Locate every blood parasite and identify its species.
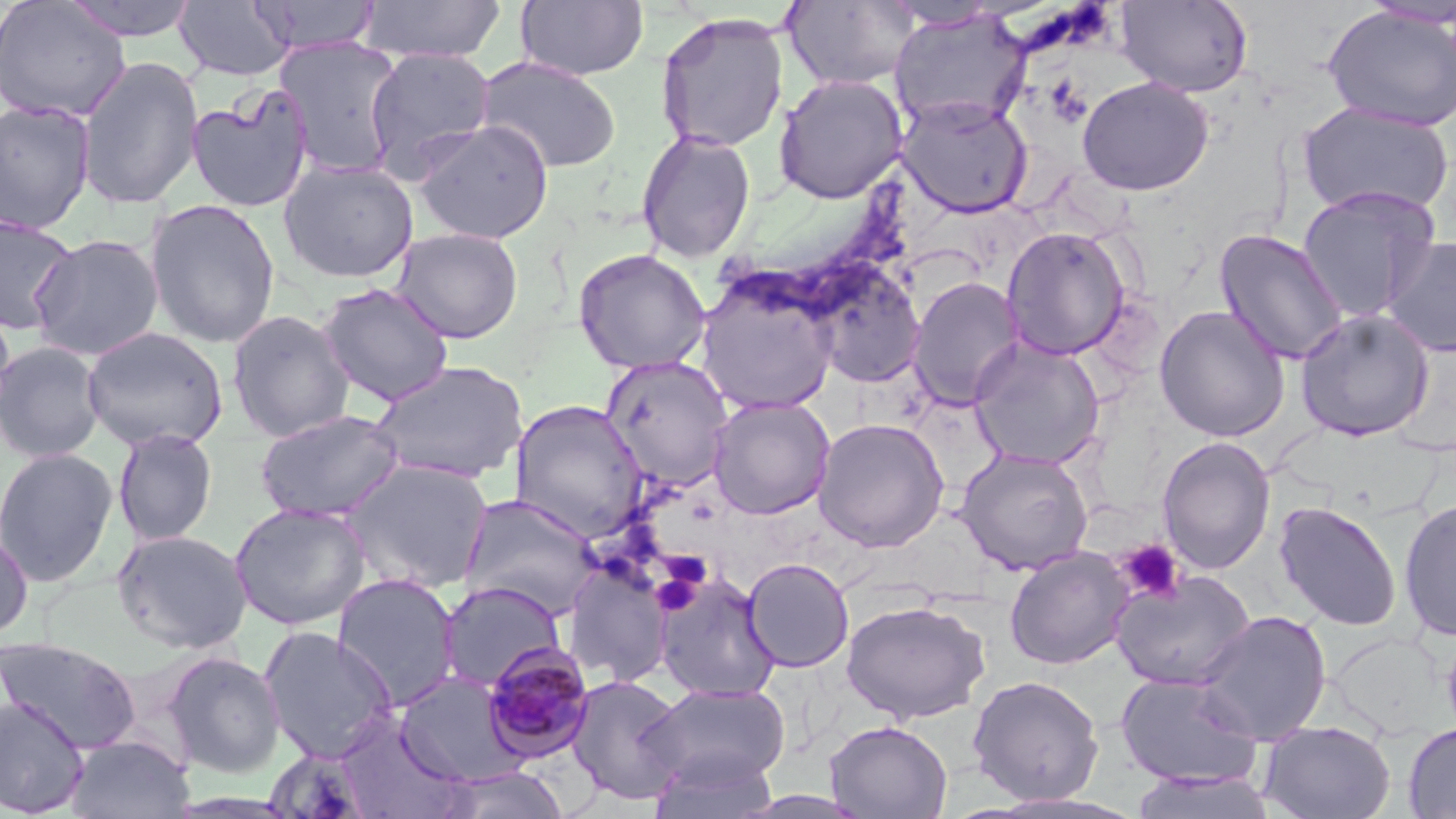
Approximate bounding boxes as [x1, y1, x2, y2] in pixels.
Plasmodium malariae-infected red blood cells: [481, 641, 595, 762].
No Plasmodium falciparum, Plasmodium ovale, Plasmodium vivax, Babesia divergens, or Trypanosoma brucei observed.

slide_level_diagnosis: Plasmodium malariae
preparation: thin blood smear
field_of_view: one of a larger specimen
uninfected_red_blood_cell_locations: 'approximate bounding boxes as [x1, y1, x2, y2] in pixels: [62, 0, 202, 42], [356, 0, 507, 62], [515, 0, 649, 81], [783, 0, 920, 91], [0, 1, 131, 124], [175, 1, 294, 82], [249, 1, 382, 55], [1115, 1, 1254, 97], [881, 2, 1009, 30], [1322, 4, 1456, 132], [889, 9, 1031, 133], [654, 11, 790, 154], [274, 36, 406, 177], [363, 46, 498, 181], [77, 56, 204, 210], [476, 56, 623, 174], [773, 73, 908, 204], [1076, 77, 1214, 196], [186, 87, 314, 213], [897, 95, 1033, 218], [0, 99, 97, 234], [1297, 102, 1454, 218], [412, 119, 554, 244], [636, 129, 757, 263], [278, 159, 419, 283], [1296, 184, 1440, 323], [144, 198, 281, 349], [0, 214, 80, 334], [1001, 226, 1131, 360], [390, 227, 524, 344], [1214, 228, 1349, 366], [28, 234, 163, 361], [1382, 236, 1456, 358], [572, 248, 712, 374], [806, 265, 926, 388], [695, 275, 841, 416], [908, 277, 1024, 410], [316, 282, 455, 408], [0, 300, 17, 427], [1153, 304, 1290, 442], [1295, 308, 1435, 441], [227, 309, 355, 442], [81, 326, 228, 452], [968, 336, 1106, 469], [0, 341, 106, 463], [600, 354, 735, 492], [369, 360, 529, 484], [707, 396, 835, 519], [510, 400, 649, 543], [254, 409, 405, 523], [812, 417, 949, 552], [112, 428, 219, 547], [1156, 436, 1276, 575], [0, 447, 119, 587], [954, 447, 1095, 575], [340, 459, 494, 593], [458, 494, 605, 620], [1399, 498, 1456, 641], [229, 501, 372, 630], [1273, 501, 1402, 631], [111, 528, 253, 655], [0, 530, 33, 640], [1004, 547, 1134, 669], [561, 555, 674, 689], [742, 558, 854, 672], [1111, 570, 1256, 691], [653, 571, 782, 702], [331, 573, 462, 711], [437, 581, 567, 693], [840, 598, 990, 724], [1195, 610, 1332, 746], [257, 626, 399, 764], [1441, 633, 1456, 739], [0, 636, 142, 755], [163, 651, 285, 778], [394, 671, 525, 785], [1114, 672, 1263, 789], [566, 674, 688, 804], [967, 675, 1105, 805], [641, 681, 792, 794], [0, 695, 91, 818], [335, 713, 470, 819], [824, 719, 953, 818], [1259, 719, 1396, 819], [1403, 722, 1456, 818], [65, 734, 194, 819], [263, 747, 375, 818], [648, 749, 781, 819], [439, 766, 570, 819], [1129, 770, 1277, 819], [981, 793, 1144, 818]'
magnification: 1000x
image_size: 1456×819 pixels
platelet_locations: 'approximate bounding boxes as [x1, y1, x2, y2] in pixels: [1116, 539, 1185, 604], [659, 552, 710, 598], [651, 571, 700, 616]'
modality: light microscopy
stain: May-Grünwald-Giemsa